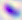

Summary:
  - Identification: Toxoplasma gondii
  - Modality: micrograph
  - Magnification: 400x